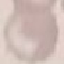

Summary:
  - Malaria status: uninfected
  - Preparation: thin blood film
  - Capture: smartphone camera at the microscope eyepiece
  - Image type: cell patch, automatically extracted from a larger field of view and resized to 64 × 64 pixels
  - Stain: Giemsa